Locate every Plasmodium falciparum-infected red blood cell.
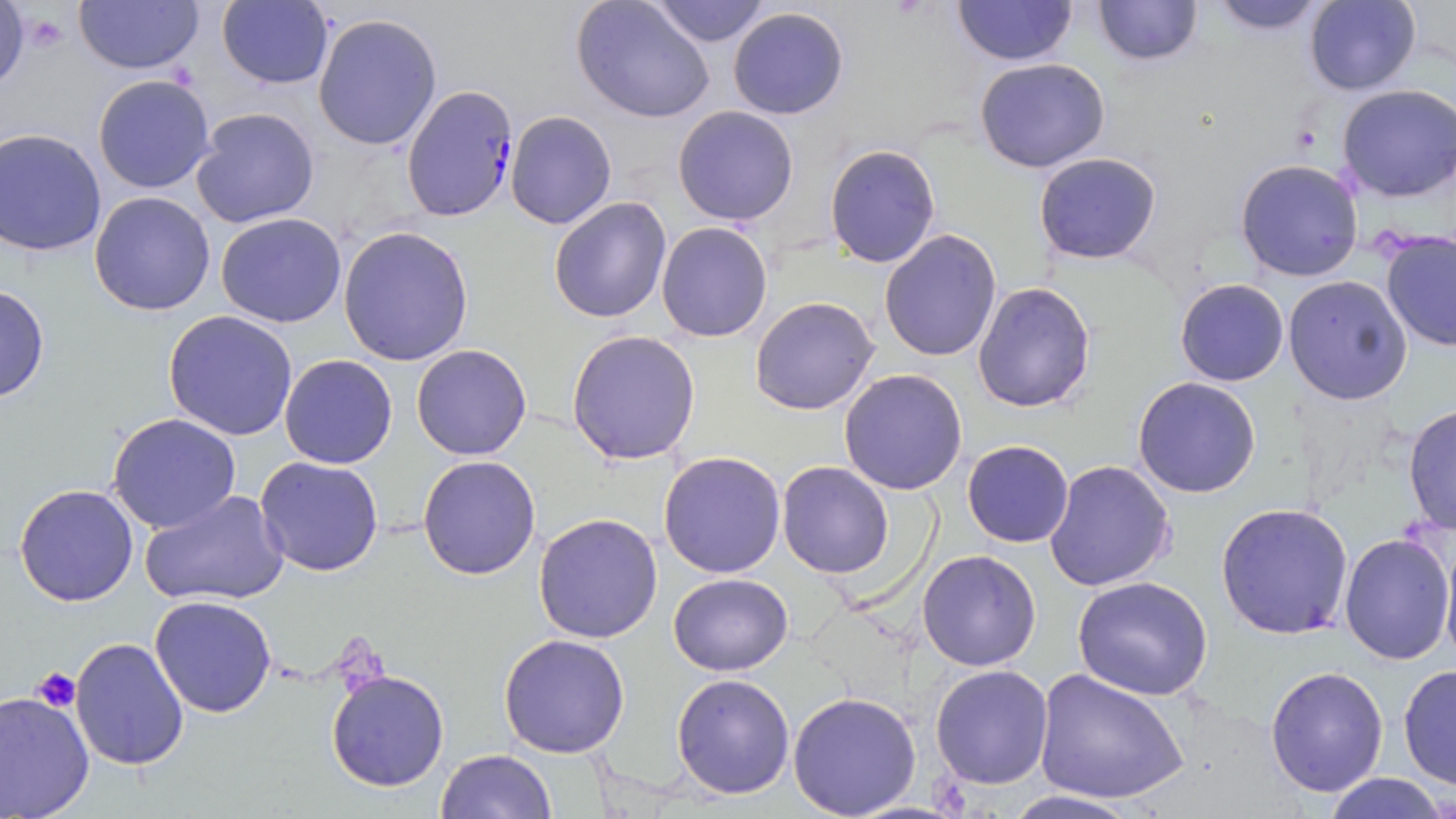

Approximate bounding boxes as (x1,y1)-(x2,y2) corner pairs in pixels.
Plasmodium falciparum-infected red blood cells: (402,84)-(521,224).

Platelet locations: (18,11)-(70,55), (32,667)-(82,713). Uninfected red blood cell locations: (73,0)-(206,76), (647,0)-(772,46), (951,0)-(1078,66), (1094,0)-(1202,67), (215,1)-(334,89), (572,1)-(716,125), (1205,1)-(1337,36), (1303,1)-(1422,94), (727,6)-(848,121), (312,13)-(444,152), (974,57)-(1109,173), (93,74)-(217,194), (1335,83)-(1456,204), (673,106)-(801,225), (191,107)-(321,228), (505,110)-(617,230), (1,128)-(106,256), (825,143)-(941,267), (1032,151)-(1163,265), (1235,159)-(1365,281), (89,191)-(217,317), (549,196)-(672,323), (215,212)-(347,328), (656,222)-(773,342), (337,225)-(475,366), (879,228)-(1002,361), (1379,230)-(1456,353), (1283,275)-(1413,406), (1175,279)-(1288,386), (973,281)-(1096,413), (0,284)-(49,404), (750,296)-(879,415), (164,311)-(298,441), (567,329)-(701,466), (410,345)-(533,461), (279,355)-(398,470), (839,369)-(969,495), (1132,377)-(1262,498), (1403,404)-(1456,540), (106,413)-(243,534), (962,440)-(1073,548), (658,450)-(786,577), (255,454)-(384,576), (418,455)-(542,579), (1044,458)-(1176,593), (776,461)-(895,579), (14,483)-(140,606), (139,489)-(288,608), (1215,502)-(1355,639), (533,512)-(664,646), (1338,530)-(1454,666), (1440,537)-(1455,671), (916,549)-(1042,670), (667,573)-(795,675), (1069,575)-(1215,700), (148,595)-(277,718), (499,633)-(632,757), (71,638)-(190,771), (930,664)-(1054,790), (1398,664)-(1455,790), (1264,665)-(1389,797), (1034,667)-(1189,805), (325,670)-(450,793), (671,673)-(796,800), (0,691)-(96,817), (787,691)-(922,817), (435,748)-(556,818), (1321,773)-(1450,818), (998,789)-(1146,819). Slide-level diagnosis: Plasmodium falciparum. One field of a larger specimen. Light microscopy. May-Grünwald-Giemsa stain. Captured at 1000x magnification. Image is 1456×819 pixels. Thin blood film.